Name the blood parasite species.
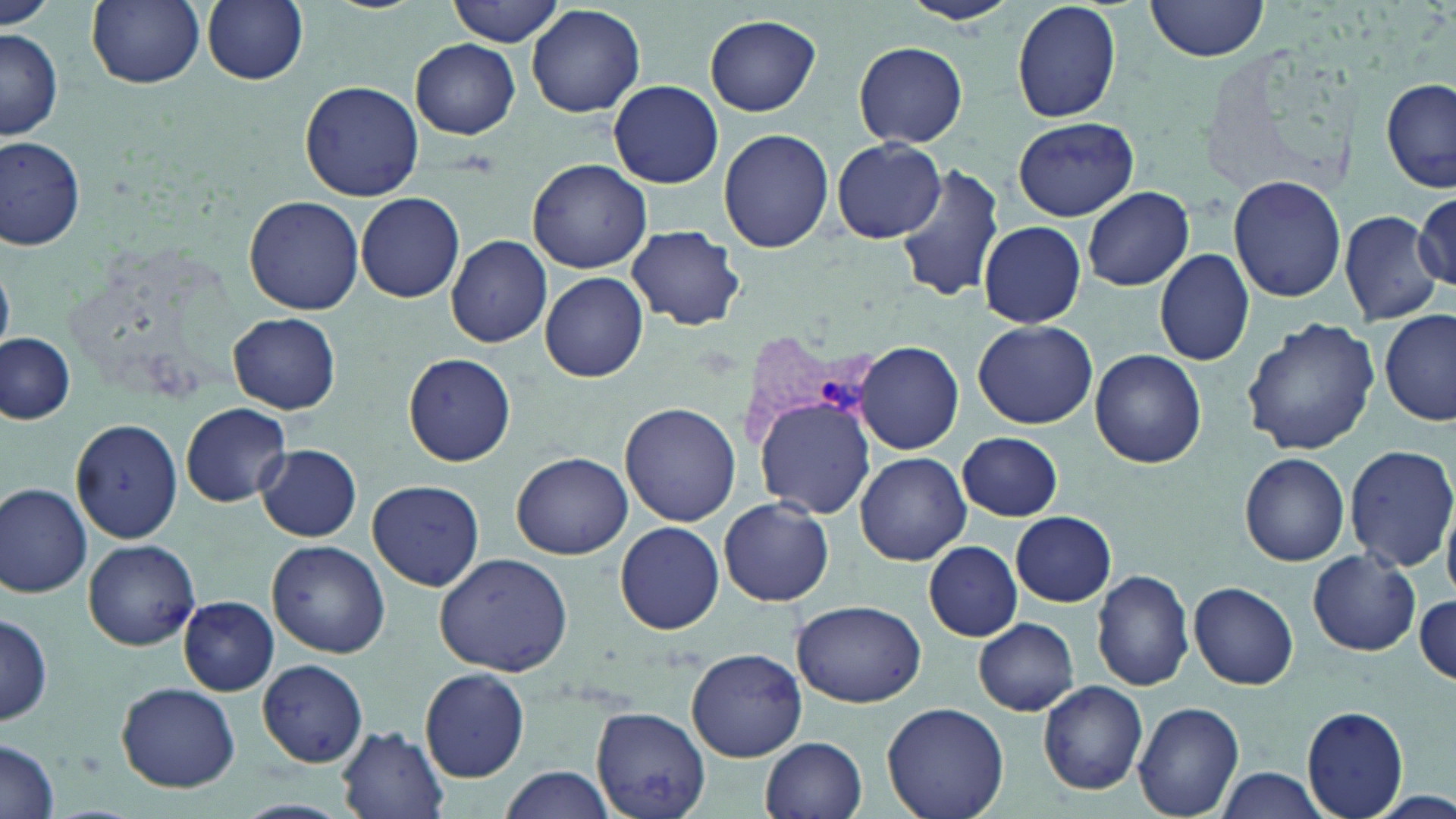
Plasmodium vivax.

Approximate bounding boxes as named x1/y1/x2/y2 corners in pixels. Plasmodium vivax-infected red blood cell locations: (x1=738, y1=335, x2=880, y2=448). Uninfected red blood cell locations: (x1=88, y1=0, x2=204, y2=90), (x1=202, y1=0, x2=308, y2=86), (x1=449, y1=0, x2=566, y2=47), (x1=899, y1=0, x2=1019, y2=28), (x1=1012, y1=0, x2=1122, y2=122), (x1=1143, y1=1, x2=1273, y2=66), (x1=1, y1=3, x2=56, y2=31), (x1=525, y1=4, x2=646, y2=118), (x1=705, y1=14, x2=820, y2=116), (x1=0, y1=26, x2=63, y2=142), (x1=411, y1=40, x2=521, y2=138), (x1=854, y1=40, x2=968, y2=148), (x1=1381, y1=76, x2=1456, y2=193), (x1=300, y1=80, x2=423, y2=202), (x1=607, y1=80, x2=723, y2=188), (x1=1012, y1=117, x2=1139, y2=220), (x1=719, y1=129, x2=834, y2=253), (x1=1, y1=134, x2=86, y2=250), (x1=832, y1=139, x2=948, y2=242), (x1=528, y1=160, x2=651, y2=274), (x1=896, y1=162, x2=1005, y2=303), (x1=1229, y1=176, x2=1345, y2=301), (x1=1081, y1=187, x2=1194, y2=291), (x1=1414, y1=191, x2=1454, y2=286), (x1=354, y1=193, x2=466, y2=303), (x1=242, y1=196, x2=365, y2=316), (x1=1340, y1=210, x2=1445, y2=327), (x1=978, y1=220, x2=1087, y2=327), (x1=627, y1=224, x2=745, y2=331), (x1=445, y1=235, x2=552, y2=348), (x1=1154, y1=248, x2=1254, y2=368), (x1=540, y1=273, x2=647, y2=381), (x1=1379, y1=311, x2=1455, y2=426), (x1=229, y1=313, x2=340, y2=414), (x1=1241, y1=316, x2=1380, y2=456), (x1=974, y1=320, x2=1097, y2=428), (x1=0, y1=333, x2=77, y2=425), (x1=855, y1=341, x2=964, y2=455), (x1=1091, y1=350, x2=1206, y2=468), (x1=404, y1=354, x2=516, y2=466), (x1=755, y1=396, x2=876, y2=517), (x1=181, y1=402, x2=294, y2=508), (x1=621, y1=403, x2=741, y2=528), (x1=68, y1=420, x2=188, y2=545), (x1=957, y1=431, x2=1064, y2=520), (x1=256, y1=443, x2=362, y2=542), (x1=1344, y1=443, x2=1456, y2=575), (x1=513, y1=452, x2=634, y2=560), (x1=856, y1=453, x2=971, y2=565), (x1=1240, y1=453, x2=1350, y2=567), (x1=367, y1=478, x2=483, y2=591), (x1=0, y1=484, x2=92, y2=598), (x1=717, y1=498, x2=834, y2=607), (x1=1009, y1=511, x2=1117, y2=606), (x1=615, y1=521, x2=724, y2=634), (x1=83, y1=538, x2=200, y2=650), (x1=268, y1=540, x2=391, y2=658), (x1=922, y1=541, x2=1022, y2=642), (x1=1306, y1=548, x2=1421, y2=655), (x1=433, y1=551, x2=576, y2=678), (x1=1093, y1=570, x2=1194, y2=692), (x1=1188, y1=582, x2=1300, y2=690), (x1=1415, y1=591, x2=1454, y2=686), (x1=179, y1=596, x2=279, y2=695), (x1=792, y1=598, x2=926, y2=707), (x1=0, y1=611, x2=52, y2=728), (x1=973, y1=618, x2=1079, y2=715), (x1=686, y1=648, x2=808, y2=762), (x1=257, y1=658, x2=368, y2=766), (x1=421, y1=667, x2=529, y2=782), (x1=1037, y1=680, x2=1147, y2=795), (x1=116, y1=682, x2=241, y2=791), (x1=882, y1=701, x2=1009, y2=819), (x1=1135, y1=701, x2=1245, y2=819), (x1=591, y1=705, x2=711, y2=819), (x1=1301, y1=705, x2=1411, y2=819), (x1=337, y1=725, x2=450, y2=819), (x1=760, y1=737, x2=867, y2=819), (x1=0, y1=739, x2=61, y2=819), (x1=500, y1=766, x2=615, y2=819), (x1=1212, y1=767, x2=1331, y2=819). One field of a larger specimen. Thin blood smear. Image is 1456×819 pixels. Captured at 1000x magnification. Light microscopy. May-Grünwald-Giemsa stain.